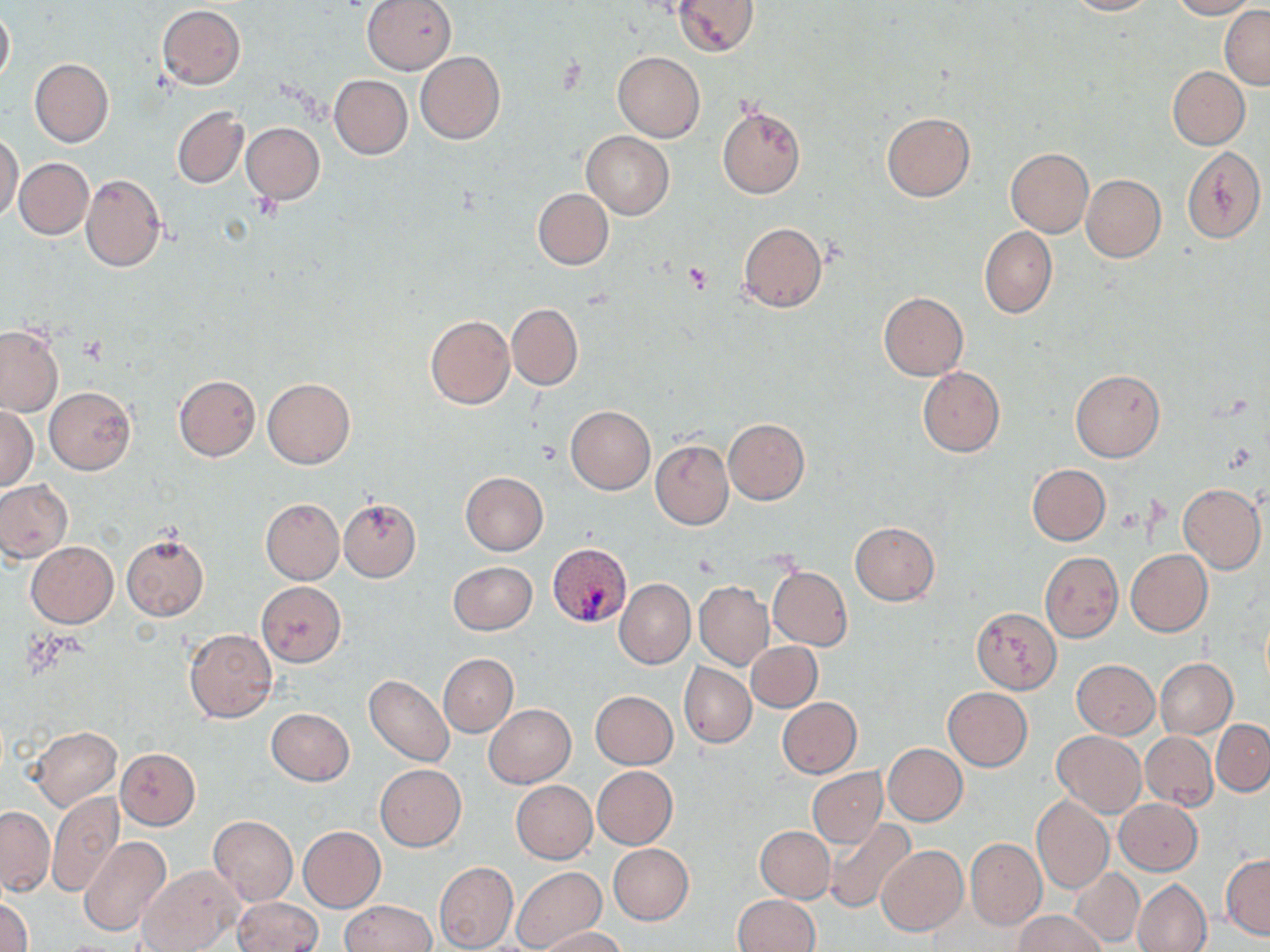

Summary:
  - Coordinate format: approximate bounding boxes as (x1, y1, x2, y2) in pixels
  - Plasmodium vivax-infected red blood cell locations: (547, 542, 633, 628)
  - Uninfected red blood cell locations: (361, 0, 457, 74), (674, 0, 759, 56), (1063, 0, 1155, 15), (1168, 0, 1255, 19), (157, 4, 246, 88), (0, 6, 13, 88), (1220, 6, 1270, 88), (415, 52, 505, 143), (613, 52, 705, 143), (30, 58, 113, 146), (1168, 67, 1249, 149), (329, 74, 413, 159), (172, 106, 248, 187), (717, 107, 806, 199), (882, 112, 975, 201), (241, 122, 324, 204), (582, 131, 675, 218), (0, 133, 24, 221), (1181, 145, 1266, 244), (1005, 147, 1093, 238), (13, 157, 93, 239), (81, 174, 166, 273), (1081, 174, 1166, 262), (533, 188, 614, 270), (738, 222, 826, 312), (979, 226, 1057, 319), (878, 292, 967, 381), (506, 303, 583, 390), (424, 315, 515, 409), (0, 325, 65, 416), (917, 367, 1005, 456), (1070, 369, 1165, 462), (174, 375, 261, 461), (262, 377, 354, 468), (45, 387, 135, 474), (565, 405, 655, 495), (0, 406, 38, 490), (723, 417, 809, 504), (651, 440, 734, 529), (1026, 464, 1110, 545), (460, 472, 548, 555), (0, 480, 72, 562), (1178, 482, 1266, 573), (261, 498, 344, 583), (339, 499, 421, 580), (849, 521, 940, 605), (121, 531, 209, 621), (25, 541, 118, 628), (1126, 549, 1212, 635), (1040, 551, 1123, 642), (448, 561, 538, 636), (767, 566, 852, 650), (615, 578, 695, 669), (257, 581, 346, 666), (695, 582, 773, 669), (972, 608, 1061, 693), (184, 628, 278, 723), (747, 642, 821, 712), (439, 654, 518, 736), (1154, 658, 1237, 738), (1072, 660, 1159, 739), (679, 662, 756, 747), (364, 674, 454, 767), (943, 687, 1032, 770), (591, 691, 678, 768), (777, 697, 862, 778), (483, 704, 575, 788), (266, 708, 354, 786), (1212, 720, 1270, 795), (27, 725, 121, 812), (1053, 731, 1146, 817), (1141, 732, 1217, 810), (882, 743, 967, 825), (115, 748, 200, 829), (374, 764, 466, 850), (593, 767, 678, 848), (807, 768, 887, 847), (511, 781, 597, 863), (47, 792, 124, 898), (1031, 796, 1114, 895), (1125, 798, 1206, 952), (1114, 799, 1203, 875), (0, 806, 54, 894), (208, 815, 297, 906), (822, 819, 915, 915), (298, 826, 386, 912), (755, 826, 835, 903), (79, 836, 171, 937), (966, 838, 1045, 929), (608, 844, 695, 925), (877, 845, 967, 936), (1221, 852, 1270, 939), (434, 861, 518, 951), (138, 864, 243, 952), (511, 866, 606, 952), (1070, 867, 1145, 946), (1132, 878, 1212, 952), (732, 894, 819, 952), (0, 895, 33, 952), (233, 898, 323, 951), (340, 900, 435, 951), (1014, 911, 1105, 952), (538, 926, 626, 951)
  - Platelet locations: (683, 263, 712, 292)
  - Slide-level diagnosis: Plasmodium vivax
  - Preparation: thin blood smear
  - Image size: 1270×952 pixels
  - Magnification: 1000x
  - Field of view: single
  - Stain: May-Grünwald-Giemsa
  - Modality: optical microscopy